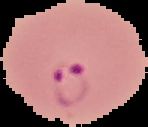
Malaria status: parasitized. From a thin blood smear. The area outside the segmented cell region is set to black. Image is 148×127 pixels.